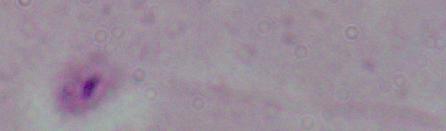
magnification: 1000x
modality: micrograph
identification: Leishmania